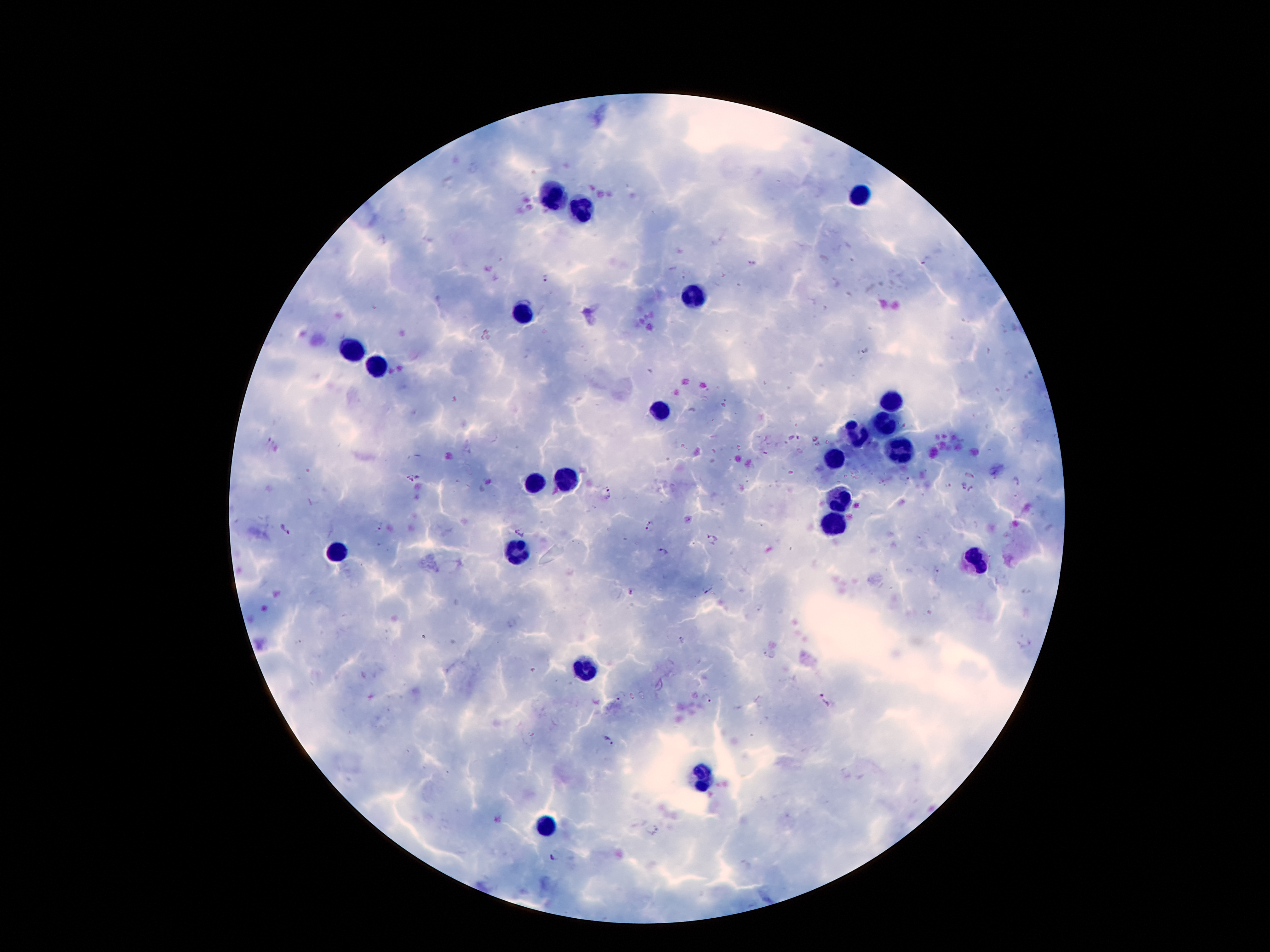

coordinate format = approximate centers as [x, y] in pixels
leukocyte locations = [556, 195], [859, 195], [586, 206], [691, 296], [523, 313], [352, 350], [381, 368], [892, 399], [657, 408], [886, 422], [858, 435], [903, 445], [838, 460], [567, 477], [537, 481], [842, 502], [835, 519], [336, 552], [519, 552], [972, 555], [586, 668], [703, 775], [546, 825]
malaria parasite locations = [925, 258], [545, 277], [969, 474], [409, 477], [904, 477], [1015, 480], [960, 486], [972, 491], [610, 493], [648, 525], [380, 527], [284, 530], [518, 530], [712, 538], [662, 553], [937, 574], [707, 588], [630, 591], [681, 639], [768, 653], [621, 695], [707, 698], [825, 701], [609, 741], [651, 829], [555, 855]
preparation = thick peripheral-blood smear
stain = Giemsa
patient malaria status = infected with Plasmodium falciparum
magnification = 100x
image size = 1270×952 pixels
capture = smartphone camera through the microscope eyepiece
field of view = one from this slide